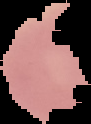
Segmented cell region on a black background. Image is 91×124 pixels. Result: no malaria parasites detected. From a thin blood film.